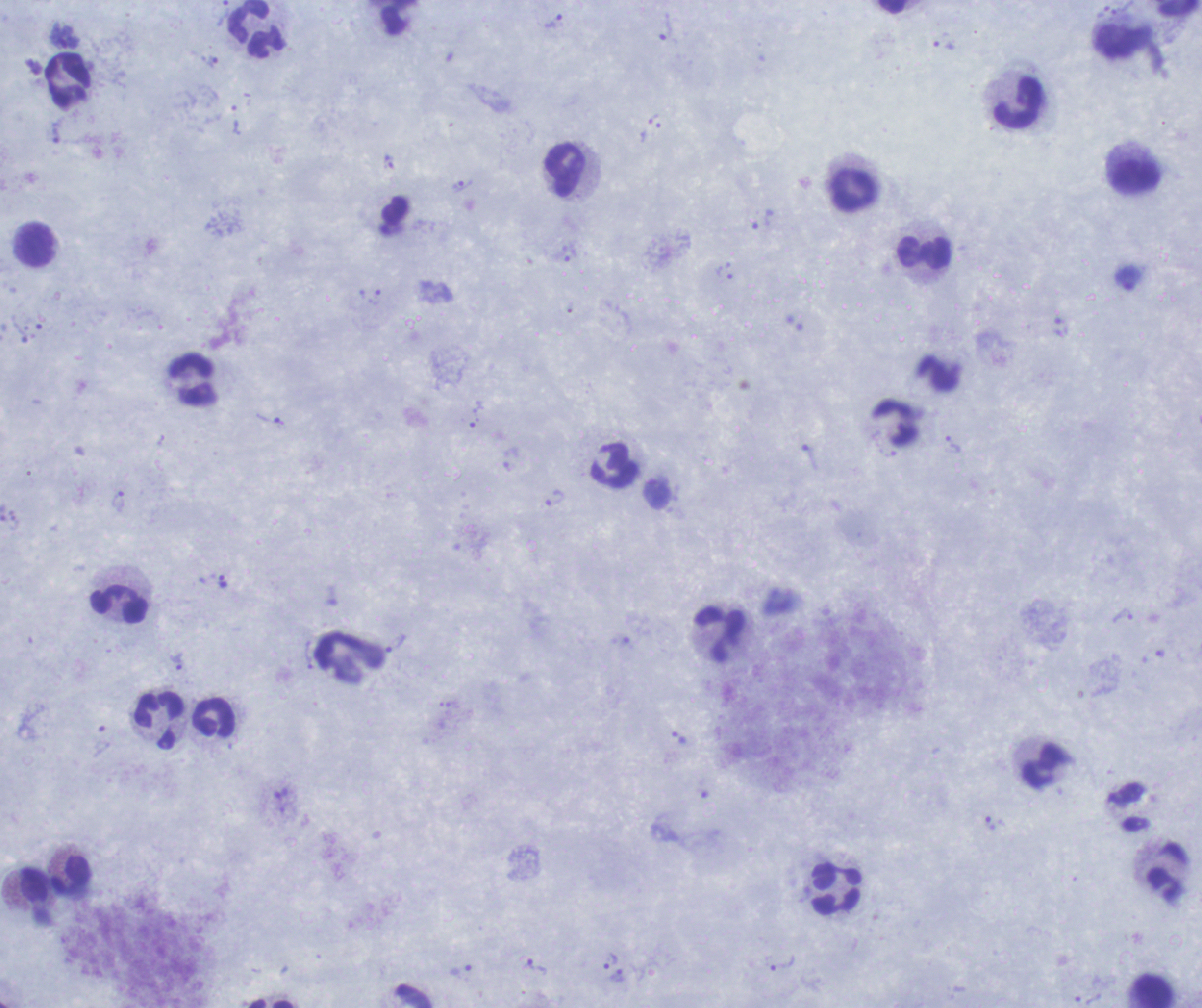

One field from this slide. Image is 1202×1008 pixels. Thick blood smear. Romanowsky stain.